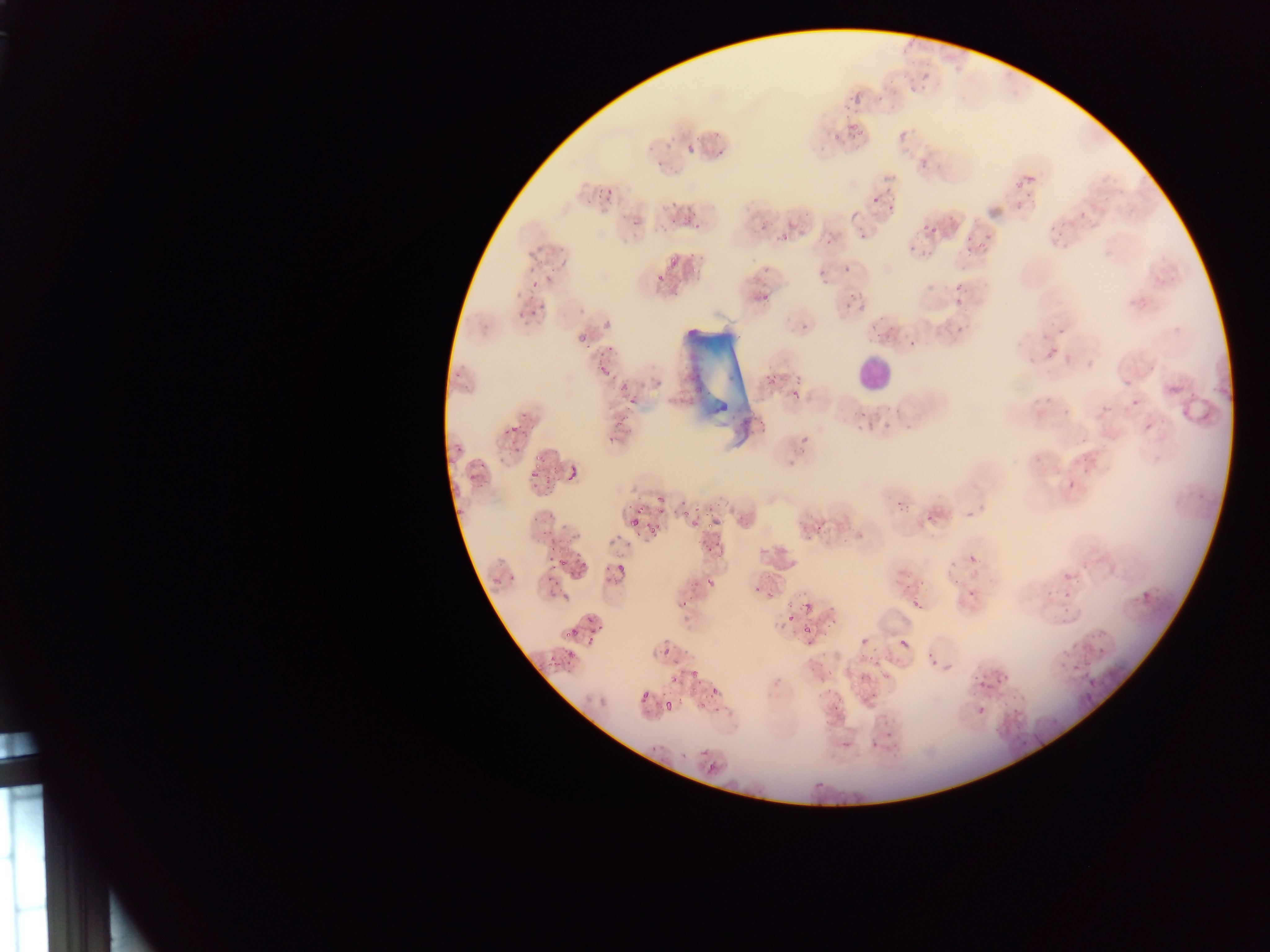

leukocyte locations = approximate bounding boxes as (left, top, right, bottom) in pixels: (853, 353, 893, 393)
malaria parasite locations = approximate bounding boxes as (left, top, right, bottom) in pixels: (901, 35, 922, 56), (911, 70, 929, 87), (836, 89, 864, 106), (874, 89, 879, 98), (887, 118, 922, 140), (830, 122, 858, 140), (685, 133, 706, 154), (664, 140, 674, 150), (705, 155, 722, 160), (1014, 170, 1032, 189), (879, 181, 900, 203), (595, 187, 618, 205), (871, 195, 879, 204), (663, 213, 689, 230), (623, 214, 644, 231), (909, 216, 944, 243), (754, 225, 763, 234), (959, 229, 983, 252), (782, 232, 795, 247), (823, 233, 840, 248), (527, 246, 552, 264), (671, 251, 683, 266), (843, 260, 853, 277), (817, 264, 832, 283), (644, 273, 665, 292), (527, 283, 540, 294), (754, 285, 777, 304), (949, 285, 970, 304), (846, 290, 867, 309), (520, 308, 549, 325), (792, 314, 820, 335), (574, 319, 595, 336), (1040, 331, 1069, 360), (909, 340, 917, 348), (685, 346, 707, 379), (595, 356, 613, 377), (757, 357, 785, 389), (448, 365, 465, 381), (794, 365, 814, 397), (616, 384, 627, 396), (1163, 385, 1190, 411), (1025, 390, 1051, 409), (1124, 396, 1136, 412), (629, 400, 636, 408), (743, 405, 764, 430), (855, 408, 879, 425), (513, 427, 529, 443), (603, 429, 628, 450), (804, 429, 814, 439), (454, 432, 469, 459), (507, 447, 519, 464), (465, 462, 483, 483), (528, 465, 545, 486), (564, 468, 576, 480), (1054, 478, 1075, 498), (894, 489, 915, 513), (651, 503, 663, 514), (458, 505, 465, 516), (679, 507, 689, 519), (919, 507, 938, 524), (629, 512, 643, 528), (529, 513, 541, 527), (709, 514, 719, 523), (693, 515, 702, 525), (807, 530, 817, 543), (541, 535, 558, 553), (700, 536, 718, 557), (963, 544, 1001, 575), (570, 547, 592, 574), (612, 557, 622, 575), (560, 558, 572, 568), (943, 560, 964, 583), (502, 566, 521, 584), (709, 575, 721, 590), (1140, 575, 1179, 611), (543, 579, 557, 598), (969, 581, 986, 598), (752, 582, 776, 602), (674, 590, 692, 607), (783, 592, 811, 631), (909, 593, 925, 610), (1047, 597, 1068, 620), (579, 608, 605, 626), (565, 623, 584, 640), (586, 630, 598, 649), (814, 632, 823, 644), (856, 633, 871, 645), (653, 634, 680, 653), (891, 639, 909, 651), (921, 651, 942, 667), (555, 653, 575, 675), (1054, 655, 1076, 673), (873, 659, 904, 689), (690, 663, 705, 675), (978, 667, 1009, 684), (1079, 670, 1099, 687), (668, 671, 684, 688), (710, 687, 721, 697), (589, 688, 626, 715), (640, 693, 650, 703), (966, 696, 984, 732), (663, 699, 673, 710), (697, 701, 707, 712), (969, 716, 985, 729), (871, 732, 884, 744), (651, 738, 671, 758), (698, 748, 707, 756), (707, 764, 716, 774) | approximate (x, y) pixel centers of objects too small to bound: (486, 580)
country = Ghana
capture = mobile-phone photograph through a microscope
image size = 1270×952 pixels
field of view = single
preparation = thin blood smear